Identify the parasite.
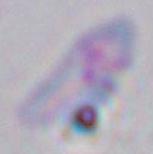

This is Toxoplasma gondii.

Summary:
  - Modality: micrograph
  - Magnification: 1000x